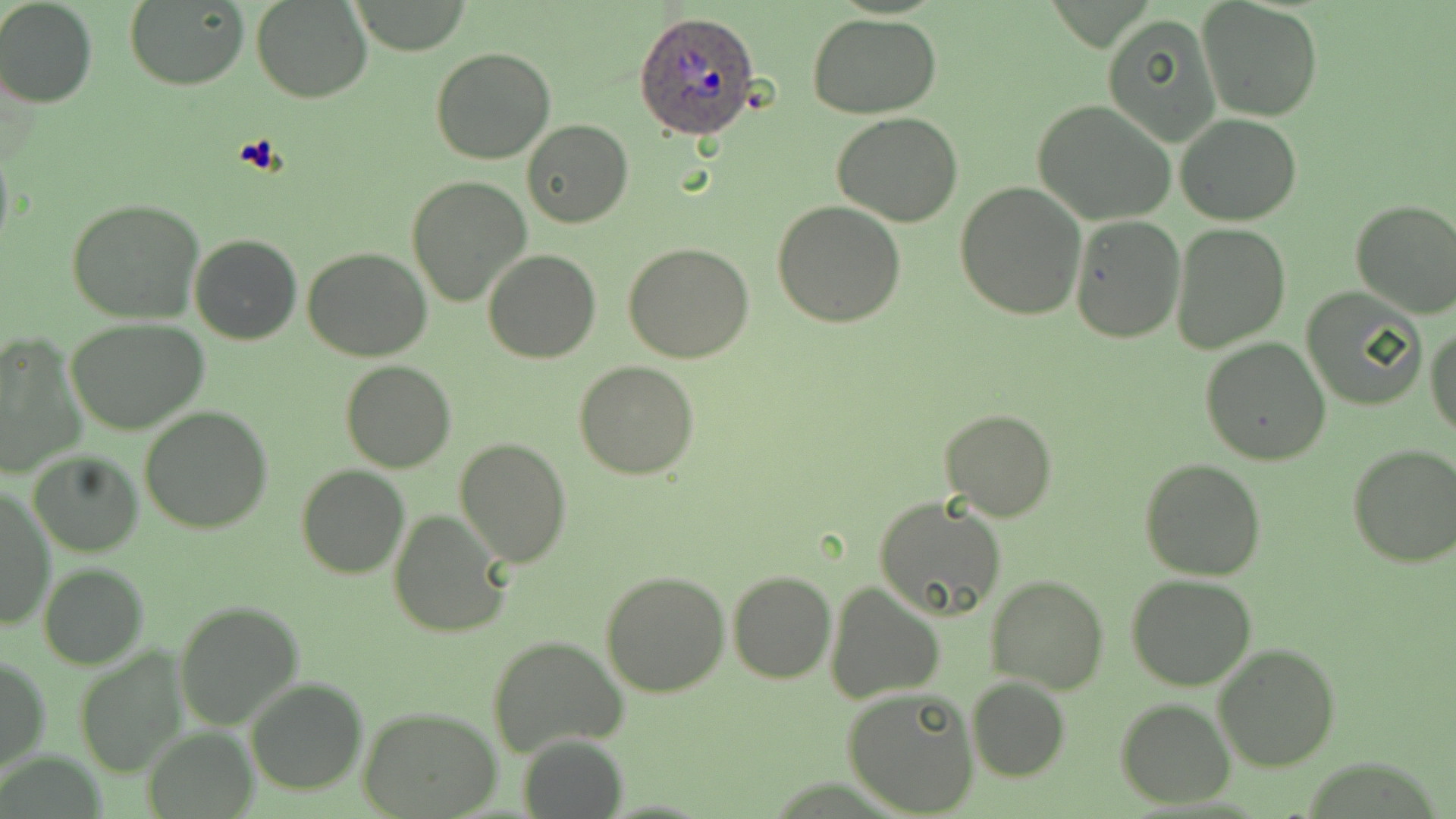
Approximate bounding boxes as named x1/y1/x2/y2 corners in pixels. Uninfected red blood cell locations: (x1=2, y1=0, x2=97, y2=107), (x1=348, y1=0, x2=475, y2=54), (x1=1197, y1=0, x2=1324, y2=120), (x1=124, y1=1, x2=248, y2=90), (x1=251, y1=1, x2=373, y2=102), (x1=805, y1=13, x2=941, y2=118), (x1=1101, y1=14, x2=1220, y2=145), (x1=431, y1=46, x2=557, y2=165), (x1=1031, y1=100, x2=1176, y2=225), (x1=831, y1=110, x2=963, y2=227), (x1=1174, y1=113, x2=1303, y2=225), (x1=521, y1=120, x2=633, y2=227), (x1=0, y1=137, x2=14, y2=266), (x1=405, y1=175, x2=532, y2=306), (x1=955, y1=182, x2=1087, y2=319), (x1=66, y1=199, x2=203, y2=323), (x1=1350, y1=200, x2=1456, y2=319), (x1=772, y1=201, x2=905, y2=327), (x1=1068, y1=215, x2=1187, y2=343), (x1=1172, y1=224, x2=1291, y2=352), (x1=189, y1=233, x2=301, y2=346), (x1=623, y1=243, x2=755, y2=364), (x1=303, y1=246, x2=433, y2=362), (x1=483, y1=248, x2=600, y2=363), (x1=1299, y1=288, x2=1425, y2=410), (x1=64, y1=319, x2=209, y2=436), (x1=1426, y1=324, x2=1456, y2=439), (x1=0, y1=333, x2=85, y2=476), (x1=1200, y1=337, x2=1332, y2=465), (x1=340, y1=361, x2=455, y2=473), (x1=574, y1=361, x2=701, y2=479), (x1=139, y1=406, x2=273, y2=533), (x1=939, y1=408, x2=1058, y2=522), (x1=455, y1=438, x2=571, y2=569), (x1=1346, y1=444, x2=1456, y2=568), (x1=27, y1=450, x2=142, y2=556), (x1=1139, y1=457, x2=1267, y2=580), (x1=296, y1=466, x2=410, y2=580), (x1=1, y1=487, x2=54, y2=633), (x1=873, y1=496, x2=1006, y2=623), (x1=388, y1=507, x2=511, y2=638), (x1=39, y1=563, x2=149, y2=669), (x1=601, y1=570, x2=731, y2=698), (x1=727, y1=571, x2=835, y2=683), (x1=986, y1=574, x2=1110, y2=693), (x1=1126, y1=574, x2=1258, y2=692), (x1=825, y1=581, x2=944, y2=703), (x1=174, y1=600, x2=304, y2=730), (x1=488, y1=634, x2=627, y2=757), (x1=1213, y1=642, x2=1342, y2=771), (x1=74, y1=646, x2=188, y2=777), (x1=0, y1=655, x2=49, y2=775), (x1=245, y1=677, x2=368, y2=797), (x1=967, y1=677, x2=1070, y2=781), (x1=842, y1=687, x2=979, y2=818), (x1=1116, y1=697, x2=1236, y2=806), (x1=357, y1=704, x2=502, y2=818), (x1=145, y1=728, x2=256, y2=817), (x1=517, y1=734, x2=630, y2=819). Plasmodium ovale-infected red blood cell locations: (x1=635, y1=9, x2=764, y2=139). Platelet locations: (x1=235, y1=134, x2=286, y2=176). Slide-level diagnosis: Plasmodium ovale. Captured at 1000x magnification. Thin blood film. Light microscopy. One field of a larger specimen. Image is 1456×819 pixels. May-Grünwald-Giemsa-stained preparation.